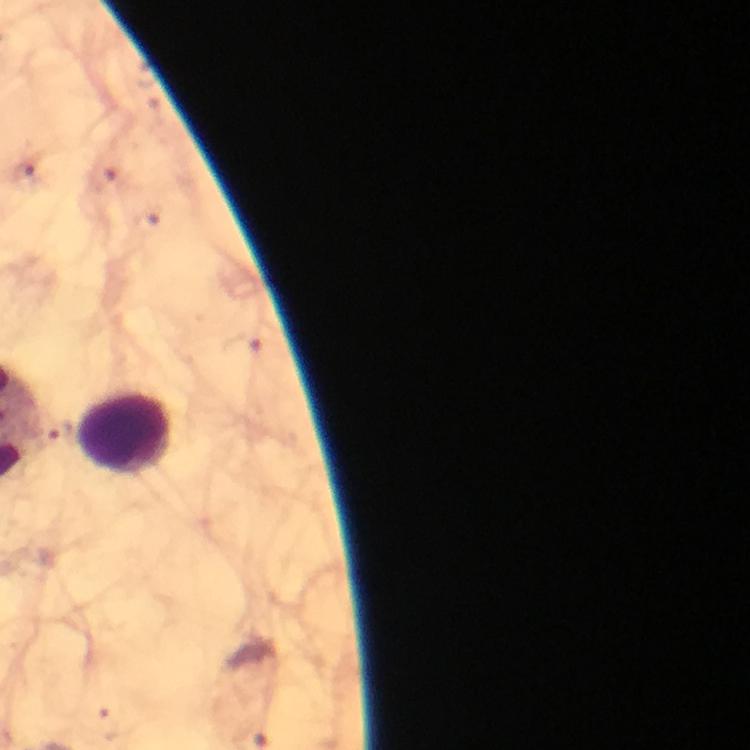
Approximate object centers, in pixels from the top-left corner. Leukocyte locations: (x=126, y=435). Plasmodium parasite locations: (x=22, y=170), (x=105, y=177), (x=146, y=222), (x=245, y=344), (x=110, y=725). Image is 750×750 pixels. A crop from one field of view. Giemsa-stained preparation. From a malaria diagnostic workup. Thick blood smear. Immersion oil applied. Smartphone photograph taken through a microscope. 100x magnification.